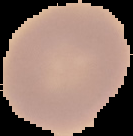
result = no malaria parasites detected
image type = cell region segmented out of the field of view; surrounding area masked to black
image size = 133×136 pixels
preparation = thin blood smear